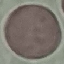

Result: no malaria parasites seen. Cell patch, automatically extracted from a larger field of view and resized to 64 × 64 pixels. Giemsa stain. Thin blood film. Acquired by smartphone through the microscope eyepiece.